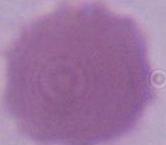

An erythrocyte is seen. 1000x magnification. Micrograph.